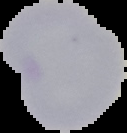
image type = cell region segmented out of the field of view; surrounding area masked to black
result = no Plasmodium parasites seen
image size = 127×133 pixels
preparation = thin blood film